Give the position of every Plasmodium parasite.
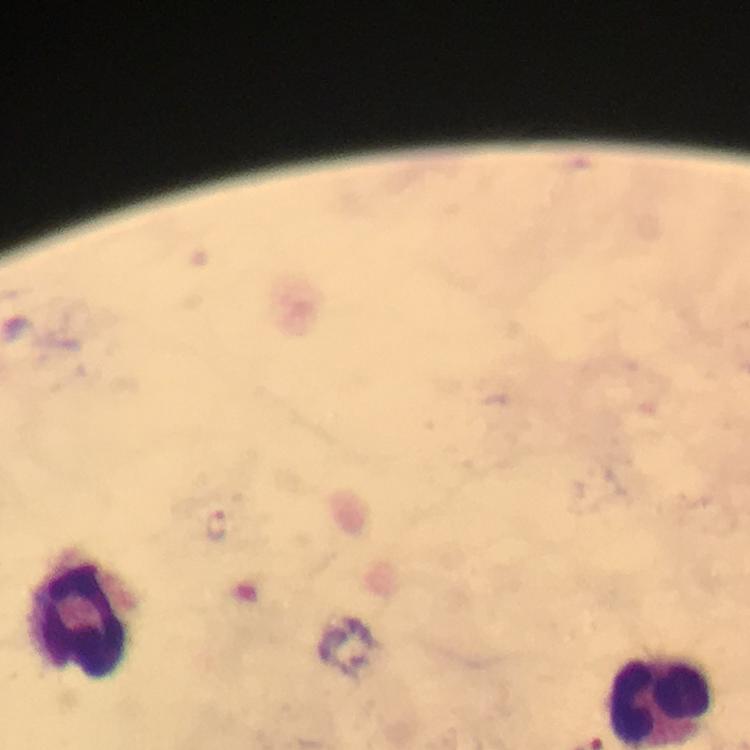

Approximate centers as {x, y} in pixels.
Plasmodium parasites: {218, 528}.

immersion_oil: used
cropped_from: a single field of view
magnification: 100x
preparation: thick blood smear
image_size: 750×750 pixels
capture: smartphone photograph through a microscope
stain: Giemsa
context: from a malaria diagnostic workup
leukocyte_locations: 'approximate centers as {x, y} in pixels: {73, 618}, {662, 702}'